Assess this cell for malaria.
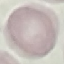

It is uninfected.

preparation = thin smear
image type = cell patch, automatically extracted from a larger field of view and resized to 64 × 64 pixels
capture = smartphone through the microscope eyepiece
stain = Giemsa